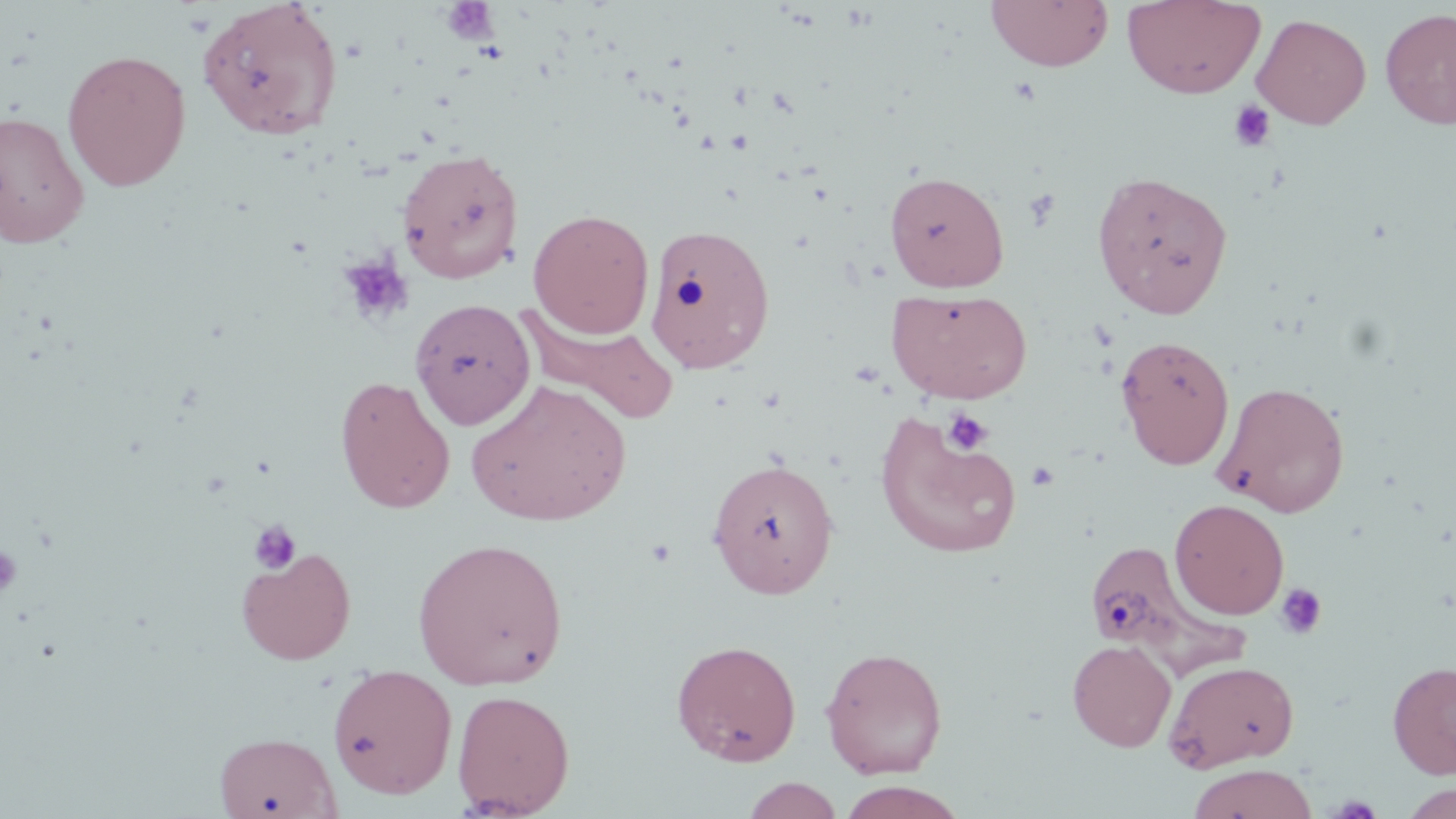
slide-level diagnosis = no evidence of blood parasites
platelet locations = approximate bounding boxes as (x1,y1)-(x2,y2) corner pairs in pixels: (442,1)-(499,44), (1228,100)-(1277,152), (1022,187)-(1061,231), (336,252)-(414,327), (942,407)-(993,455), (1027,461)-(1061,491), (249,521)-(301,574), (0,544)-(23,600), (1274,582)-(1328,640)
stain = May-Grünwald-Giemsa
uninfected red blood cell locations = approximate bounding boxes as (x1,y1)-(x2,y2) corner pairs in pixels: (985,0)-(1114,72), (1122,0)-(1266,99), (197,1)-(344,142), (1380,7)-(1456,130), (1252,13)-(1372,129), (62,49)-(192,191), (0,110)-(90,247), (397,148)-(524,283), (1091,169)-(1233,320), (884,170)-(1010,292), (528,208)-(654,338), (645,222)-(776,374), (886,287)-(1032,404), (410,298)-(536,430), (516,306)-(680,426), (1115,335)-(1235,470), (335,375)-(455,514), (466,380)-(631,527), (1214,380)-(1350,517), (875,416)-(1023,559), (707,457)-(840,599), (1170,499)-(1289,619), (412,536)-(568,690), (1082,537)-(1250,676), (237,547)-(356,665), (671,638)-(802,765), (1067,639)-(1177,752), (820,646)-(948,779), (1164,659)-(1300,772), (1387,660)-(1456,778), (327,662)-(458,799), (451,688)-(575,817), (215,731)-(340,818), (1187,763)-(1320,819), (742,776)-(844,818), (836,781)-(970,819), (1398,782)-(1455,817)
field of view = single
preparation = thin blood smear
modality = light microscopy
image size = 1456×819 pixels
magnification = 1000x